State the preparation type.
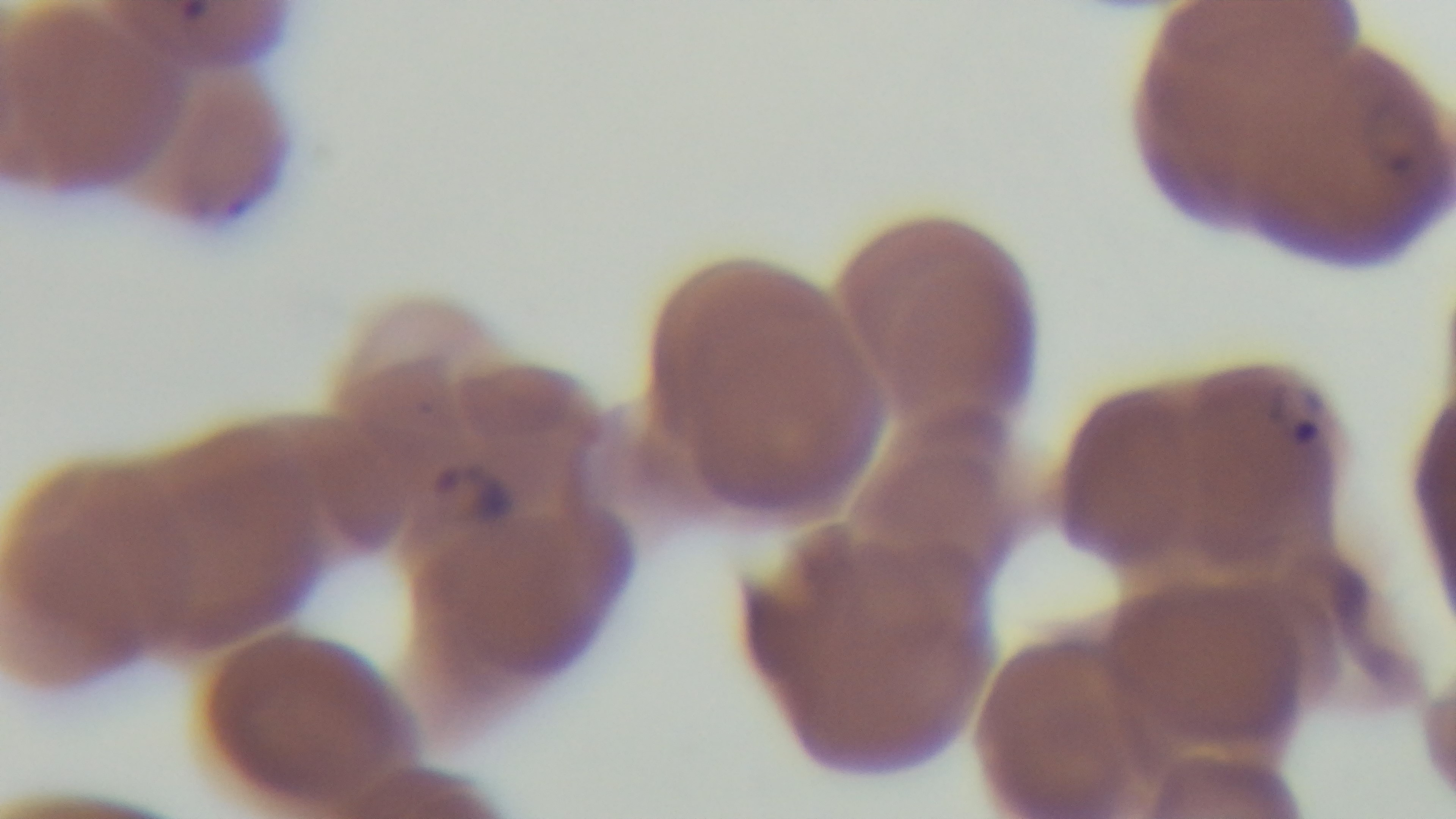

A thin smear.

Light microscopy. Oil-immersion objective, 100x. Malaria status: positive. One field from the slide. Giemsa-stained. Captured with a mounted 4K digital camera.